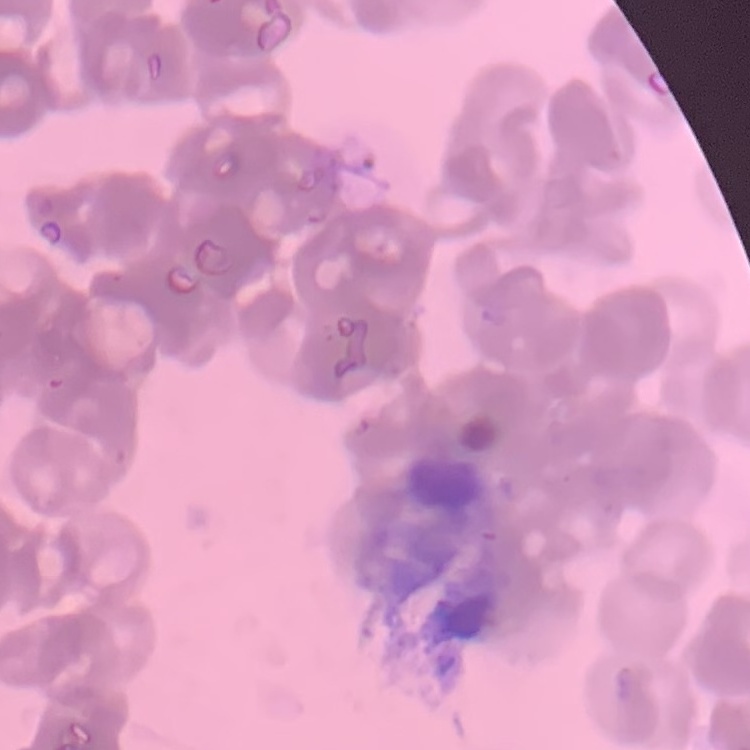

erythrocyte_morphology: rouleaux formation
preparation: thin blood smear
stain: Field's or Giemsa
image_type: square crop of a larger photomicrograph